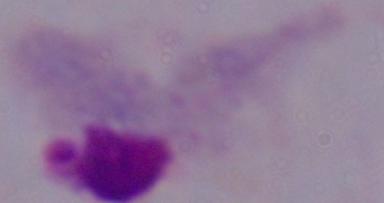
A trichomonad is seen. Photomicrograph. 1000x magnification.